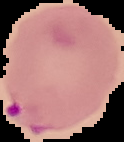
Summary:
  - Result: Plasmodium parasites identified
  - Image type: segmented cell region with the area outside set to black
  - Image size: 124×142 pixels
  - Preparation: thin blood film